Report the malaria status of this cell.
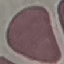

It is uninfected.

capture = smartphone camera at the microscope eyepiece
stain = Giemsa
preparation = thin blood smear
image type = cell patch, automatically extracted from a larger field of view and resized to 64 × 64 pixels